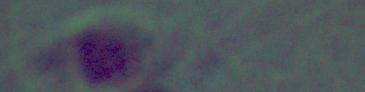
{
  "modality": "micrograph",
  "identification": "Leishmania",
  "magnification": "1000x"
}